Give the extent of all Plasmodium ovale-infected red blood cells.
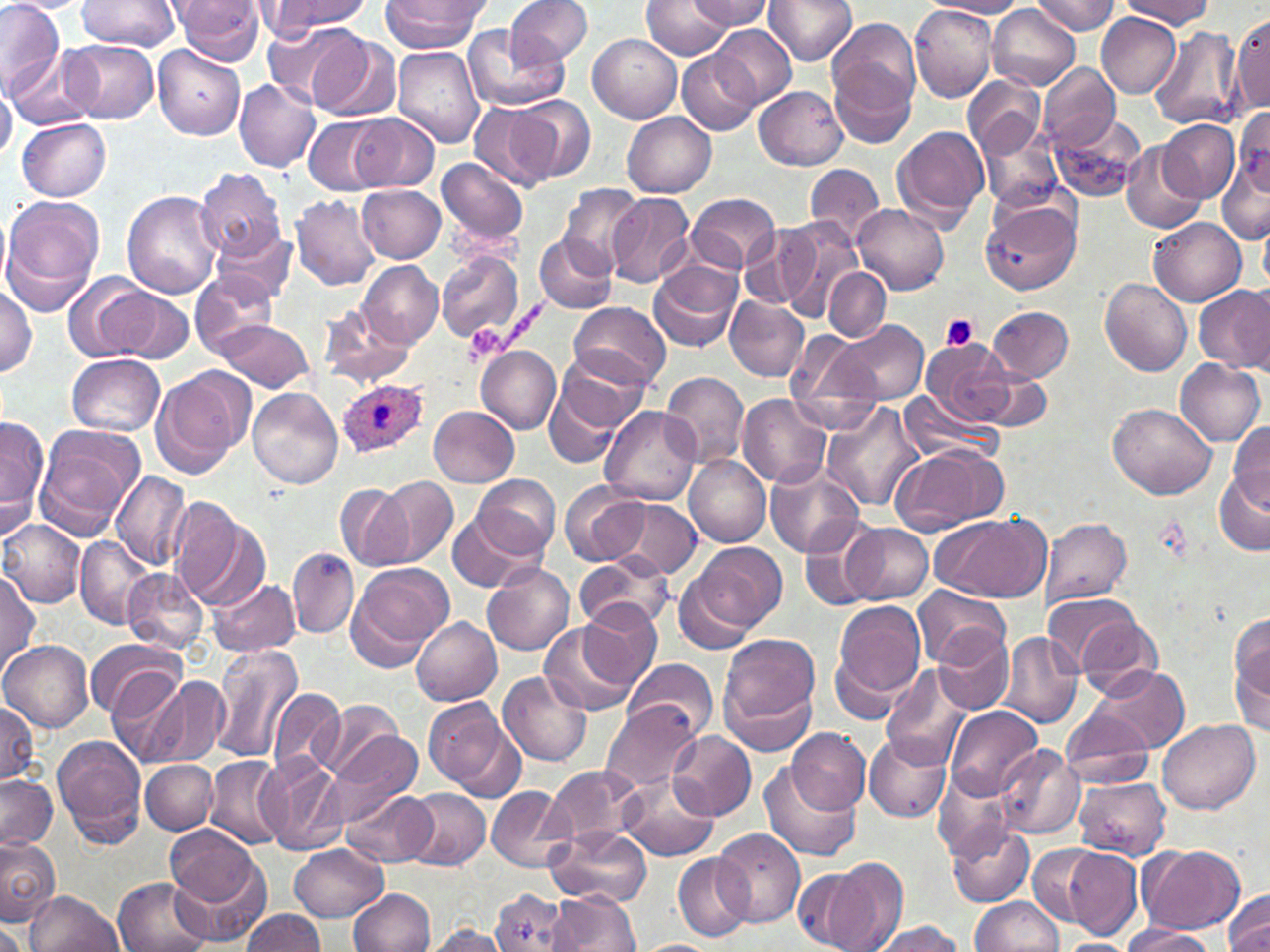
Approximate bounding boxes as [x1, y1, x2, y2] in pixels.
Plasmodium ovale-infected red blood cells: [337, 380, 428, 459].

slide-level diagnosis = Plasmodium ovale
platelet locations = approximate bounding boxes as [x1, y1, x2, y2] in pixels: [941, 314, 978, 350], [464, 324, 508, 364]
magnification = 1000x
modality = optical microscopy
preparation = thin blood film
field of view = single
stain = May-Grünwald-Giemsa
uninfected red blood cell locations = approximate bounding boxes as [x1, y1, x2, y2] in pixels: [3, 0, 83, 14], [80, 0, 180, 52], [173, 0, 266, 66], [382, 0, 485, 53], [503, 0, 592, 68], [690, 0, 772, 30], [763, 0, 857, 65], [926, 0, 1027, 17], [1031, 0, 1121, 36], [1119, 0, 1214, 28], [0, 1, 65, 97], [262, 1, 370, 36], [643, 1, 732, 60], [909, 4, 997, 102], [987, 7, 1080, 89], [1231, 12, 1269, 116], [1097, 15, 1179, 97], [829, 18, 920, 112], [262, 23, 362, 109], [711, 25, 796, 109], [460, 26, 565, 115], [1149, 27, 1240, 130], [307, 32, 400, 122], [589, 35, 681, 122], [64, 39, 158, 123], [153, 45, 245, 138], [392, 45, 485, 149], [10, 47, 98, 129], [677, 50, 761, 133], [828, 57, 918, 151], [1038, 62, 1119, 149], [964, 76, 1044, 157], [234, 79, 321, 173], [0, 81, 17, 161], [754, 86, 848, 170], [509, 96, 594, 182], [470, 102, 556, 192], [623, 112, 716, 197], [1048, 112, 1148, 203], [353, 113, 438, 191], [305, 116, 387, 195], [17, 117, 113, 199], [1233, 118, 1269, 202], [1158, 120, 1240, 203], [892, 124, 990, 228], [980, 127, 1065, 215], [1121, 141, 1206, 234], [1217, 154, 1270, 244], [436, 156, 530, 249], [805, 164, 884, 245], [193, 168, 286, 262], [356, 185, 447, 262], [559, 185, 645, 275], [120, 190, 222, 300], [686, 192, 781, 274], [606, 193, 694, 288], [291, 194, 382, 290], [0, 197, 105, 313], [980, 200, 1082, 296], [853, 203, 949, 295], [776, 218, 861, 320], [1149, 218, 1245, 305], [1260, 223, 1270, 293], [740, 224, 820, 312], [215, 226, 295, 307], [534, 233, 618, 313], [435, 249, 524, 345], [358, 261, 442, 349], [649, 261, 740, 353], [824, 269, 891, 340], [189, 271, 275, 356], [64, 273, 154, 363], [1100, 277, 1194, 376], [99, 283, 192, 365], [1194, 284, 1270, 373], [0, 285, 37, 378], [726, 295, 809, 382], [569, 302, 670, 389], [318, 305, 417, 388], [987, 306, 1074, 381], [216, 318, 314, 393], [830, 319, 929, 404], [787, 329, 871, 417], [915, 340, 1018, 424], [477, 347, 560, 433], [552, 348, 652, 436], [68, 352, 166, 436], [1175, 359, 1266, 446], [976, 369, 1053, 431], [661, 371, 751, 467], [152, 372, 245, 478], [541, 372, 631, 470], [247, 386, 343, 489], [899, 392, 1000, 464], [736, 395, 831, 487], [822, 402, 923, 512], [1108, 402, 1220, 500], [601, 405, 700, 503], [429, 406, 518, 486], [1, 419, 46, 512], [1230, 423, 1269, 512], [35, 429, 138, 535], [888, 445, 1007, 535], [683, 454, 770, 547], [2, 458, 41, 546], [765, 462, 867, 559], [111, 469, 191, 568], [1214, 469, 1270, 556], [378, 474, 458, 567], [472, 474, 559, 558], [561, 481, 652, 567], [335, 483, 414, 572], [603, 497, 703, 579], [169, 501, 268, 611], [929, 511, 1052, 602], [446, 512, 540, 594], [1041, 517, 1131, 608], [1, 519, 85, 606], [799, 524, 884, 612], [841, 524, 933, 604], [77, 536, 158, 628], [690, 540, 786, 633], [288, 548, 359, 638], [576, 554, 675, 634], [484, 562, 575, 657], [347, 564, 452, 670], [676, 567, 760, 656], [124, 568, 210, 651], [0, 569, 41, 675], [209, 577, 301, 658], [913, 585, 1010, 668], [1042, 592, 1142, 677], [830, 598, 927, 709], [577, 601, 660, 687], [1067, 610, 1164, 697], [411, 616, 502, 705], [538, 619, 637, 717], [1231, 619, 1270, 728], [933, 628, 1014, 714], [997, 631, 1083, 728], [719, 632, 822, 735], [86, 637, 183, 720], [0, 639, 94, 733], [211, 641, 305, 764], [624, 658, 720, 741], [882, 665, 976, 769], [1087, 666, 1189, 756], [108, 669, 189, 766], [498, 671, 592, 767], [141, 675, 228, 769], [268, 687, 345, 779], [723, 687, 815, 755], [424, 697, 521, 797], [316, 699, 402, 782], [0, 701, 38, 787], [600, 701, 702, 794], [944, 704, 1043, 801], [1062, 708, 1154, 787], [1156, 718, 1261, 815], [326, 727, 421, 819], [787, 728, 871, 814], [666, 730, 756, 820], [865, 730, 953, 824], [53, 734, 148, 849], [994, 743, 1085, 841], [256, 756, 343, 854], [206, 757, 286, 849], [141, 760, 218, 834], [758, 762, 862, 862], [544, 765, 643, 848], [933, 772, 1014, 859], [618, 773, 719, 863], [0, 774, 57, 852], [1073, 775, 1172, 858], [485, 786, 574, 874], [402, 788, 491, 870], [342, 791, 437, 866], [946, 821, 1035, 908], [166, 824, 268, 920], [546, 826, 651, 906], [711, 828, 805, 927], [0, 835, 61, 924], [1027, 842, 1113, 926], [1136, 843, 1246, 935], [290, 844, 388, 922], [1053, 845, 1144, 940], [671, 853, 754, 942], [804, 856, 906, 952], [113, 876, 214, 952], [348, 887, 434, 951], [1224, 889, 1270, 952], [489, 890, 572, 952], [24, 891, 122, 952], [548, 891, 641, 951], [970, 897, 1066, 952], [239, 908, 326, 951], [866, 920, 965, 952], [0, 922, 27, 952], [1119, 925, 1217, 952], [422, 926, 512, 951], [1053, 939, 1138, 952], [635, 940, 722, 952]
image size = 1270×952 pixels